Assess the morphology of the red blood cells.
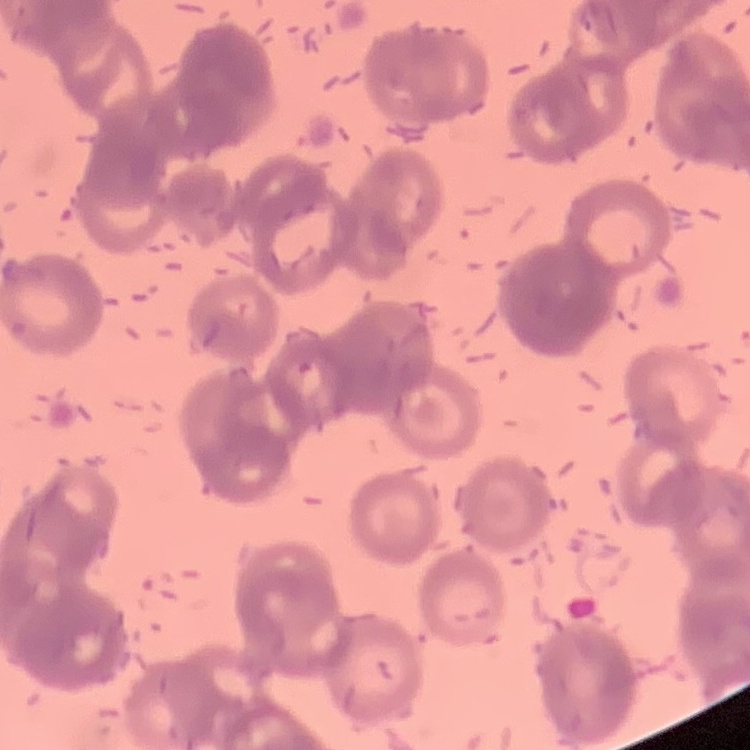

They show rouleaux formation.

image type = square crop of a larger photomicrograph
stain = Field's or Giemsa
preparation = thin blood smear